Name the parasite shown.
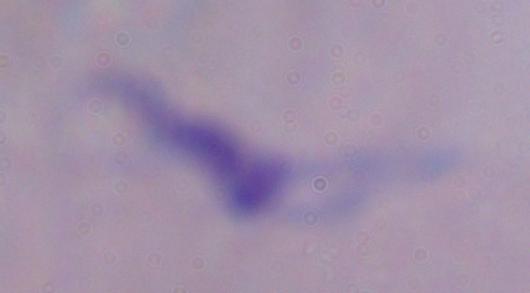

This is a trypanosome.

Photomicrograph. Captured at 1000x magnification.